Evaluate for Plasmodium parasites.
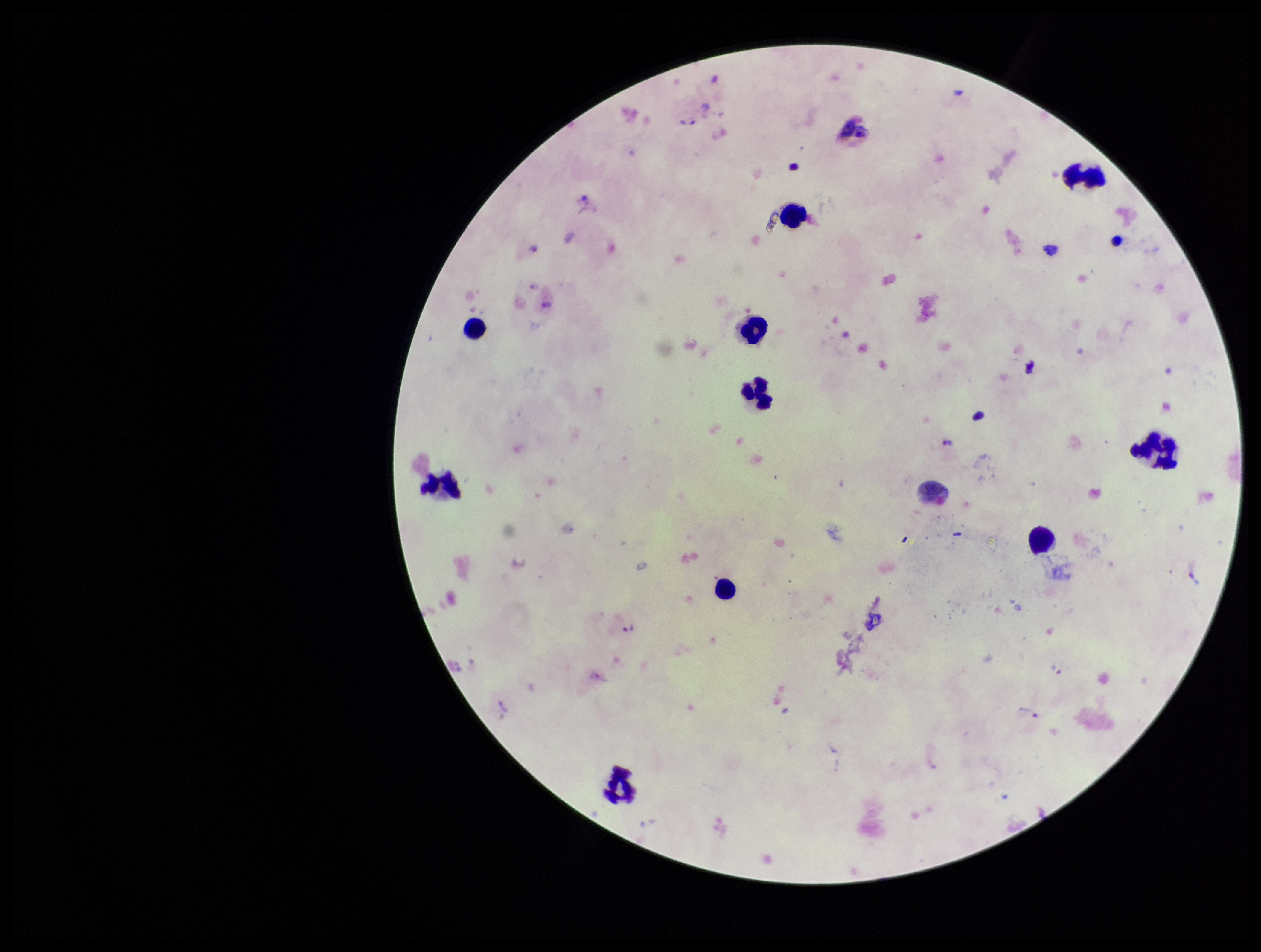
Detected.

Smartphone photograph taken through the eyepiece of a microscope. Patient malaria status: positive. Preparation: thick. One field from this slide. Image is 1261×952 pixels. Species reported for this patient: Plasmodium vivax. Stained with Giemsa. Leukocyte count: 12. Parasite count: 9.